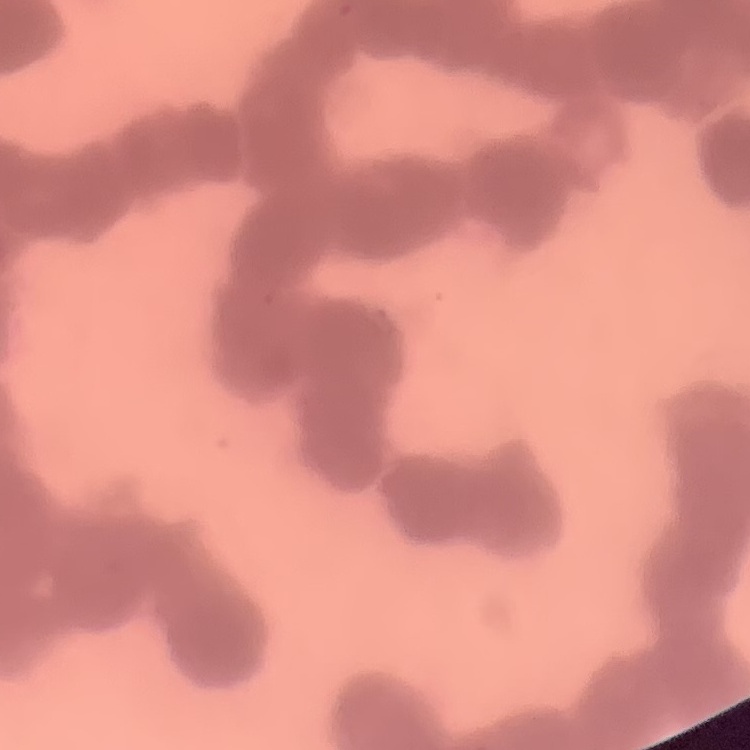
erythrocyte morphology = rouleaux formation
image type = one tile cut from a larger photomicrograph
stain = Field's or Giemsa
preparation = thin peripheral smear